State which parasite is depicted.
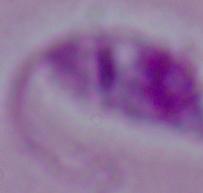

Leishmania.

Summary:
  - Magnification: 1000x
  - Modality: photomicrograph